Assess the morphology of the erythrocytes.
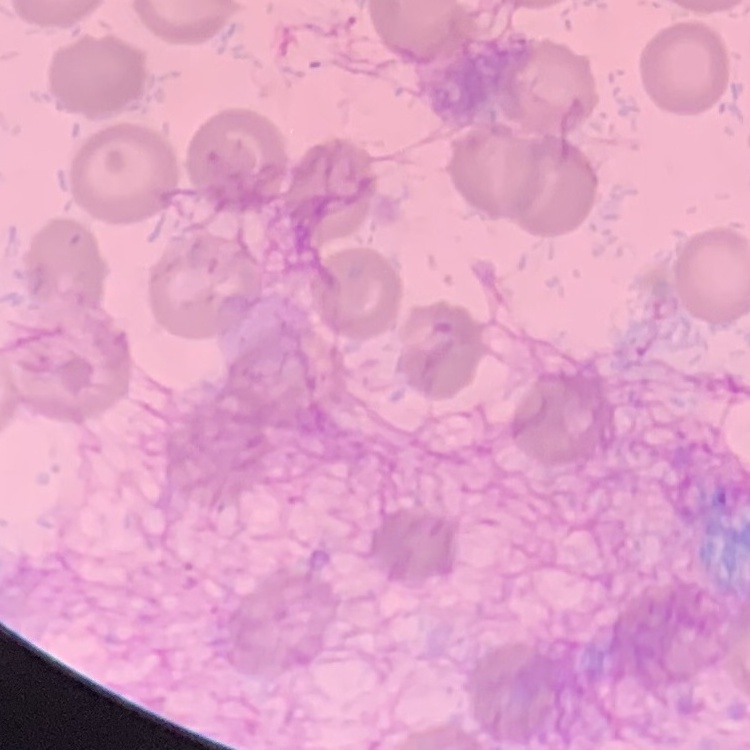

No rouleaux formation.

Stained with either Field's or Giemsa. One tile cut from a larger photomicrograph. Thin peripheral smear.